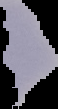

Summary:
  - Malaria status: uninfected
  - Preparation: thin blood film
  - Image type: segmented cell region on a black background
  - Image size: 58×109 pixels